Comment on the morphology of the red blood cells.
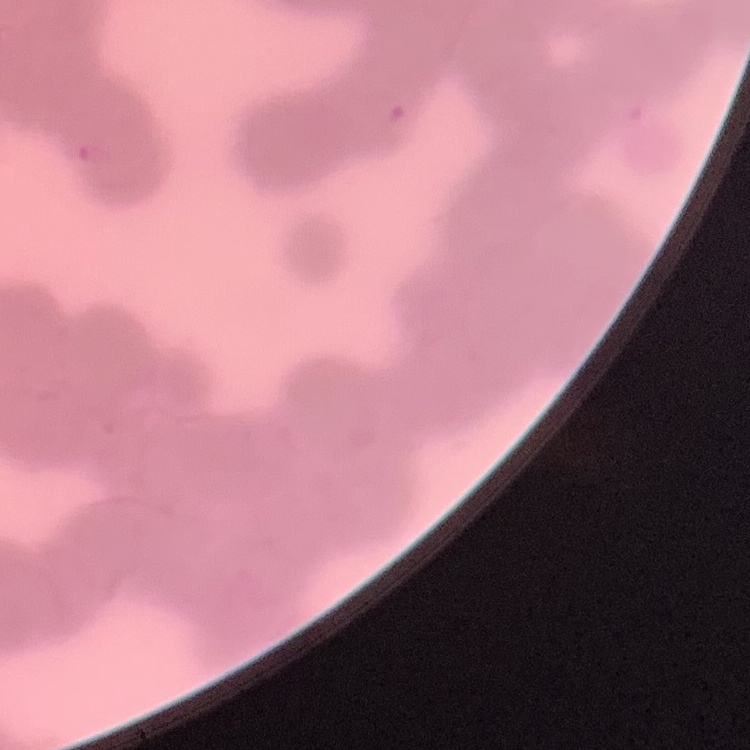
They show rouleaux formation.

Summary:
  - Preparation: thin blood smear
  - Image type: square crop of a larger photomicrograph
  - Stain: Field's or Giemsa